Assess this cell for malaria.
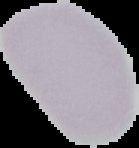
It is uninfected.

Image is 139×148 pixels. Segmented cell region on a black background. From a thin blood film.